Give the preparation type.
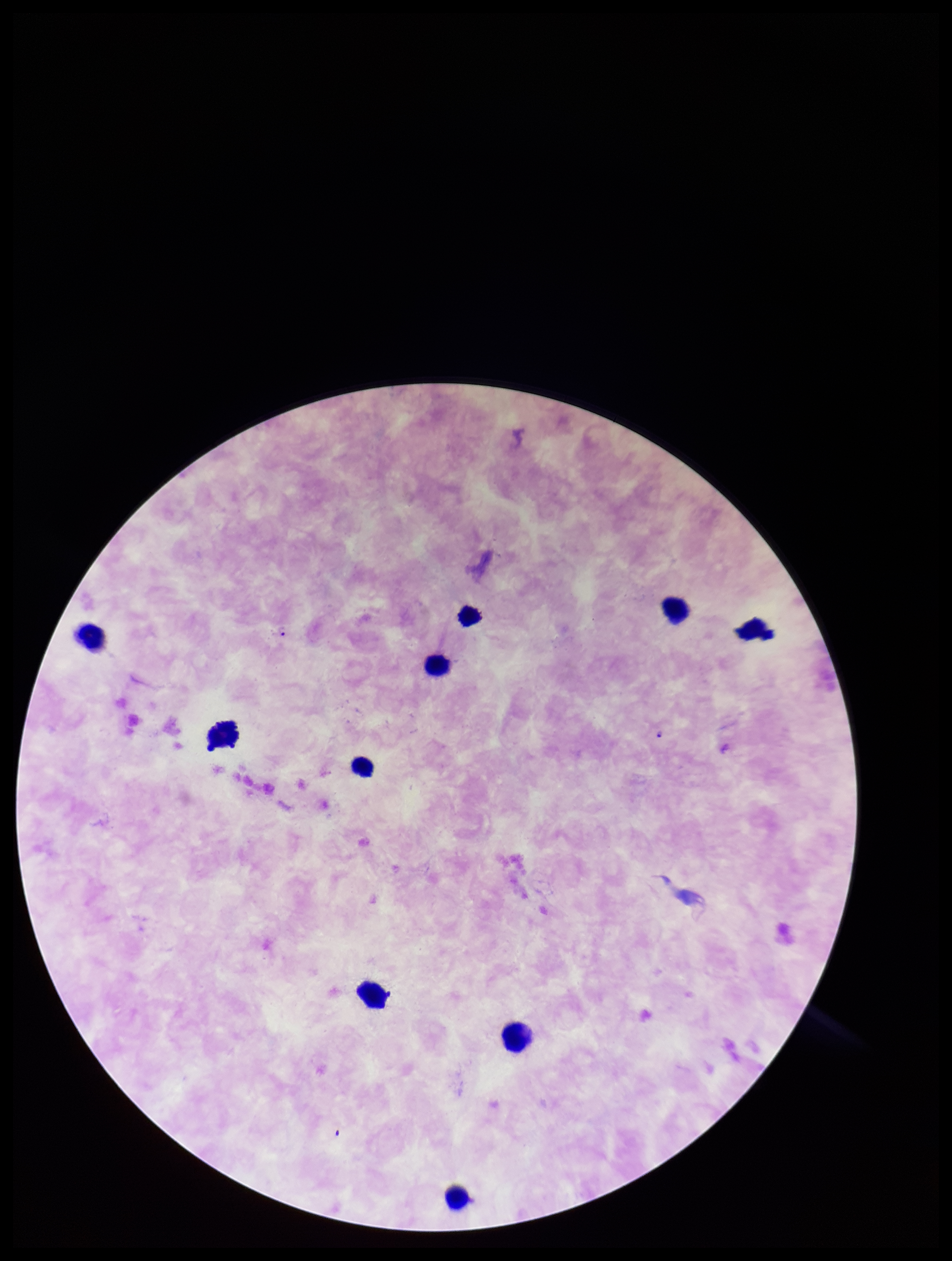
A thick smear.

Summary:
  - Parasite count: 2
  - Plasmodium parasites: identified
  - Species reported for this patient: Plasmodium falciparum
  - Capture: smartphone photograph through the microscope eyepiece
  - Patient malaria status: positive
  - Leukocyte count: 10
  - Stain: Giemsa
  - Image size: 952×1261 pixels
  - Field of view: one from this slide